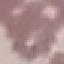
result: no malaria parasites detected
stain: Giemsa
image_type: automatically extracted cell patch, resized to 64 × 64 pixels
capture: smartphone through the microscope eyepiece
preparation: thin smear